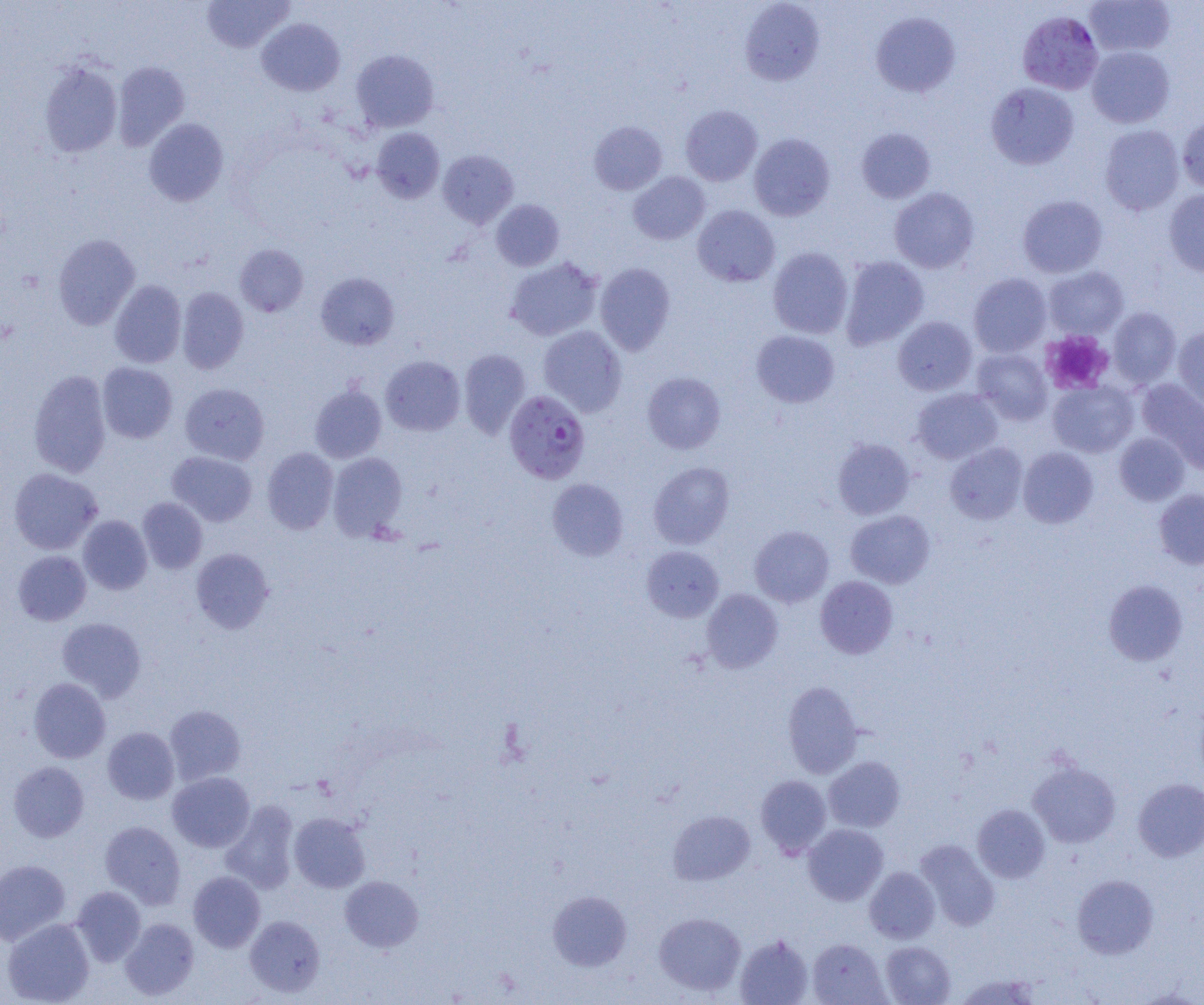

slide-level diagnosis = Plasmodium falciparum
uninfected red blood cell locations (subset) = approximate bounding boxes as (x1,y1)-(x2,y2) corner pairs in pixels: (202,0)-(294,52), (739,0)-(825,86), (1085,0)-(1175,57), (870,12)-(960,97), (256,18)-(345,96), (1086,46)-(1175,128), (350,49)-(439,132), (38,60)-(122,158), (112,61)-(190,150), (985,82)-(1079,170), (680,105)-(762,186), (1177,114)-(1204,193), (143,119)-(229,207), (589,121)-(667,195), (1099,124)-(1185,215), (371,127)-(444,203), (856,127)-(936,204), (749,133)-(835,221), (437,149)-(518,228), (628,172)-(710,245), (889,187)-(979,274), (1164,189)-(1204,277), (1017,195)-(1108,278), (491,199)-(564,271), (692,204)-(780,287), (53,233)-(140,330), (234,244)-(308,317), (768,247)-(853,338), (840,255)-(929,349), (505,257)-(603,341), (595,263)-(675,354), (1044,266)-(1129,339), (316,272)-(399,350), (968,273)-(1052,357), (109,280)-(186,368), (177,287)-(249,374), (1106,306)-(1182,388), (893,316)-(977,395), (538,326)-(627,416), (1173,326)-(1204,415), (751,330)-(840,408), (971,348)-(1052,425), (459,349)-(531,438), (381,355)-(465,436), (97,362)-(177,443), (28,369)-(112,478), (642,372)-(726,454), (1137,379)-(1204,466), (1048,381)-(1139,457), (180,382)-(270,464), (309,384)-(387,463), (912,388)-(1003,464), (1114,432)-(1189,505), (832,438)-(915,519), (945,442)-(1028,524), (262,447)-(339,534), (1018,447)-(1098,528), (167,451)-(257,526), (328,452)-(407,539), (648,462)-(734,549), (9,468)-(103,554), (547,478)-(628,561), (1154,489)-(1204,569), (137,497)-(207,574), (845,510)-(935,588), (78,515)-(152,595), (749,525)-(834,607), (641,545)-(724,622), (191,548)-(274,633), (13,550)-(92,626), (815,576)-(898,659), (1104,579)-(1188,665), (701,588)-(784,672), (57,617)-(146,701), (28,677)-(111,763), (782,681)-(864,778), (164,705)-(245,785), (102,727)-(179,804), (824,756)-(905,832), (8,761)-(89,842), (1028,762)-(1120,848), (168,772)-(255,852), (755,774)-(832,858), (1133,778)-(1204,861), (221,800)-(299,894), (973,804)-(1050,883), (668,811)-(755,884), (289,812)-(370,892), (100,820)-(186,908), (802,824)-(888,905), (915,839)-(1000,930), (0,859)-(71,945), (864,867)-(940,943), (188,871)-(265,952), (1072,874)-(1159,959), (340,876)-(423,952), (71,886)-(146,966), (548,890)-(632,971), (654,912)-(745,995), (244,915)-(325,997), (2,917)-(95,1005), (120,918)-(199,1000), (735,934)-(813,1005), (807,938)-(889,1005), (880,941)-(955,1005), (953,973)-(1041,1004)
preparation = thin blood smear
image size = 1204×1005 pixels
magnification = 1000x
Plasmodium falciparum-infected red blood cell locations (subset) = approximate bounding boxes as (x1,y1)-(x2,y2) corner pairs in pixels: (504,390)-(590,484)
platelet locations = approximate bounding boxes as (x1,y1)-(x2,y2) corner pairs in pixels: (1041,330)-(1114,395)
modality = optical microscopy
field of view = one of a larger specimen